Classify this cell by malaria status.
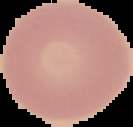

It is uninfected.

Summary:
  - Preparation: thin blood smear
  - Image type: segmented cell region with the area outside set to black
  - Image size: 133×127 pixels